Identify the blood parasite species.
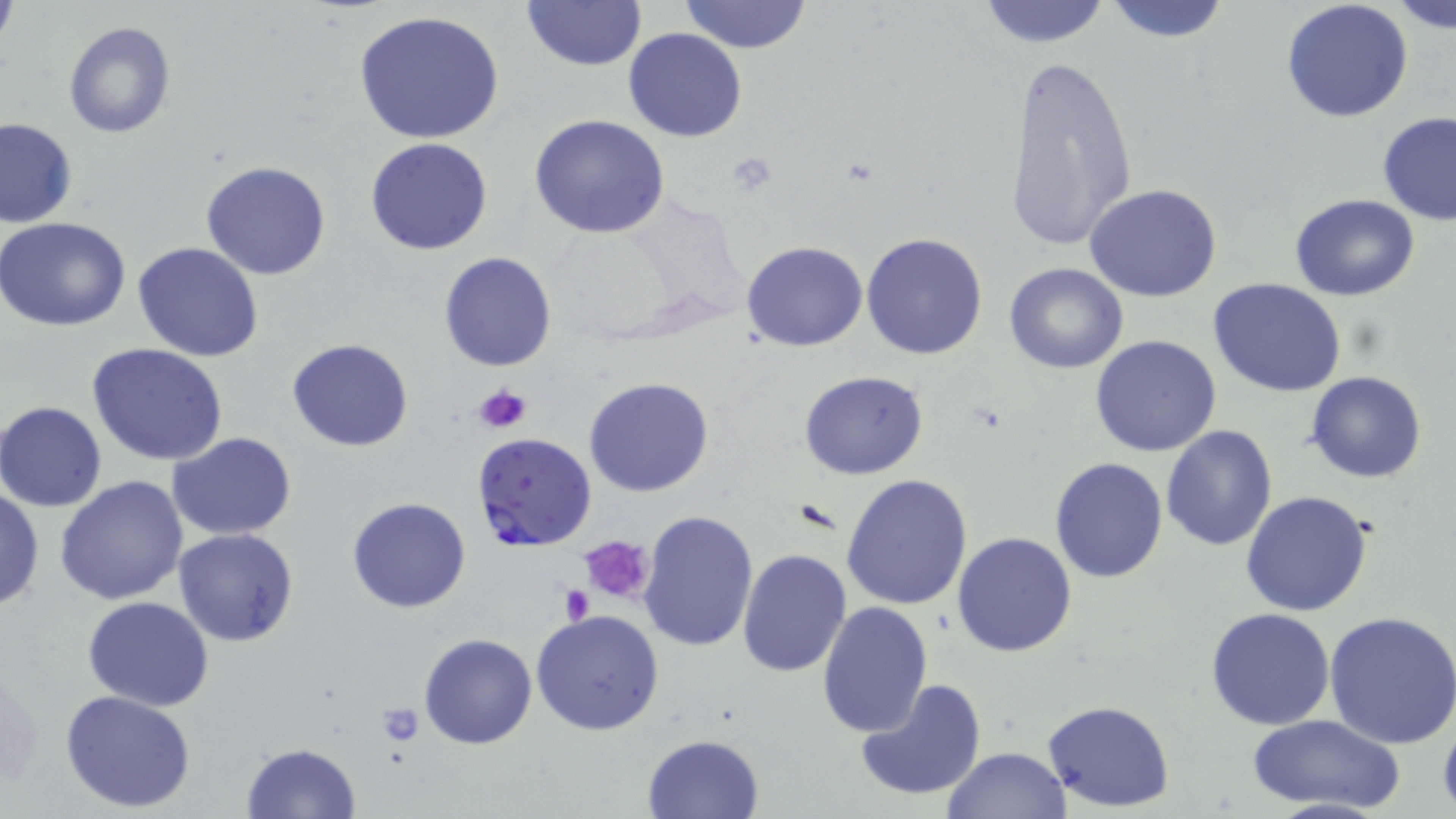
Plasmodium falciparum.

Approximate bounding boxes as (x1,y1)-(x2,y2) corner pairs in pixels. Plasmodium falciparum-infected red blood cell locations: (471,433)-(599,553). Platelet locations: (472,382)-(532,435), (582,534)-(655,604), (560,586)-(596,623), (373,703)-(424,745). Uninfected red blood cell locations: (522,0)-(645,70), (678,0)-(814,53), (1099,0)-(1234,43), (1279,0)-(1414,123), (1390,0)-(1455,33), (973,1)-(1115,48), (0,3)-(18,57), (353,10)-(506,145), (63,21)-(175,138), (624,28)-(748,144), (1003,52)-(1137,254), (1377,111)-(1456,224), (530,115)-(670,240), (1,119)-(77,229), (367,138)-(493,256), (200,162)-(331,281), (1084,183)-(1224,302), (1290,194)-(1420,301), (0,217)-(132,331), (860,232)-(989,359), (133,241)-(264,361), (741,241)-(869,351), (438,251)-(557,372), (1003,263)-(1128,373), (1207,276)-(1347,398), (1090,335)-(1223,457), (286,337)-(413,452), (87,344)-(229,466), (798,370)-(929,479), (1305,370)-(1428,484), (583,377)-(714,498), (1,401)-(108,511), (1159,425)-(1279,550), (168,433)-(297,542), (1050,457)-(1168,583), (841,473)-(973,612), (56,477)-(189,606), (0,485)-(43,612), (1240,489)-(1373,615), (346,497)-(471,614), (638,508)-(760,652), (173,528)-(301,647), (951,532)-(1077,658), (737,550)-(853,678), (83,596)-(214,711), (816,600)-(932,739), (1205,607)-(1337,731), (531,608)-(665,737), (1325,608)-(1456,749), (419,633)-(537,749), (854,677)-(988,805), (60,688)-(197,814), (1043,699)-(1176,813), (1248,713)-(1405,814), (641,733)-(765,819), (240,742)-(362,818), (941,747)-(1071,818). Image is 1456×819 pixels. One field of a larger specimen. May-Grünwald-Giemsa-stained preparation. 1000x magnification. Light microscopy. Thin blood film.